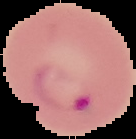
Summary:
  - Preparation: thin blood smear
  - Image size: 136×139 pixels
  - Image type: segmented cell region with the area outside set to black
  - Result: Plasmodium parasites identified